Describe the morphology of the erythrocytes.
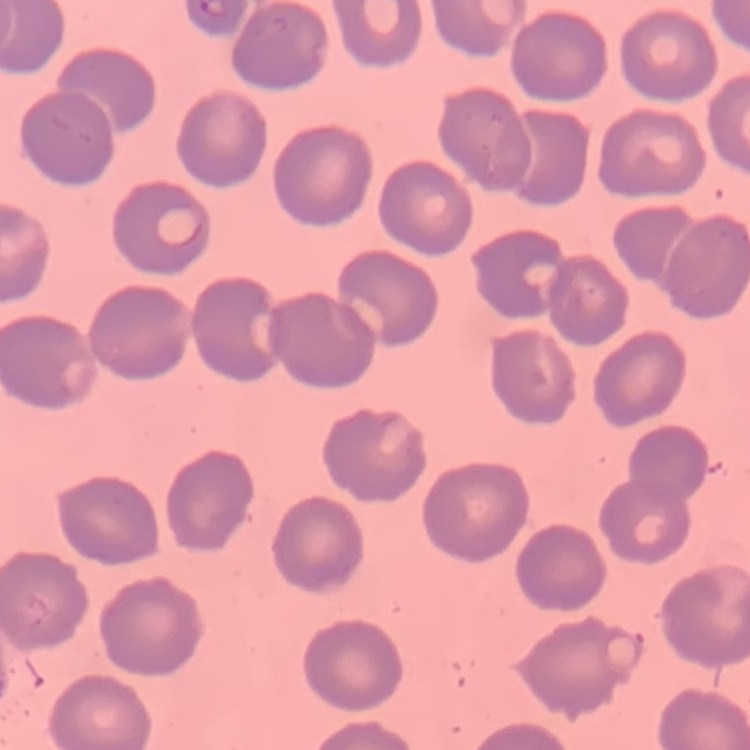
They show no rouleaux formation.

Thin blood smear. One tile cut from a larger photomicrograph. Field's or Giemsa stain.